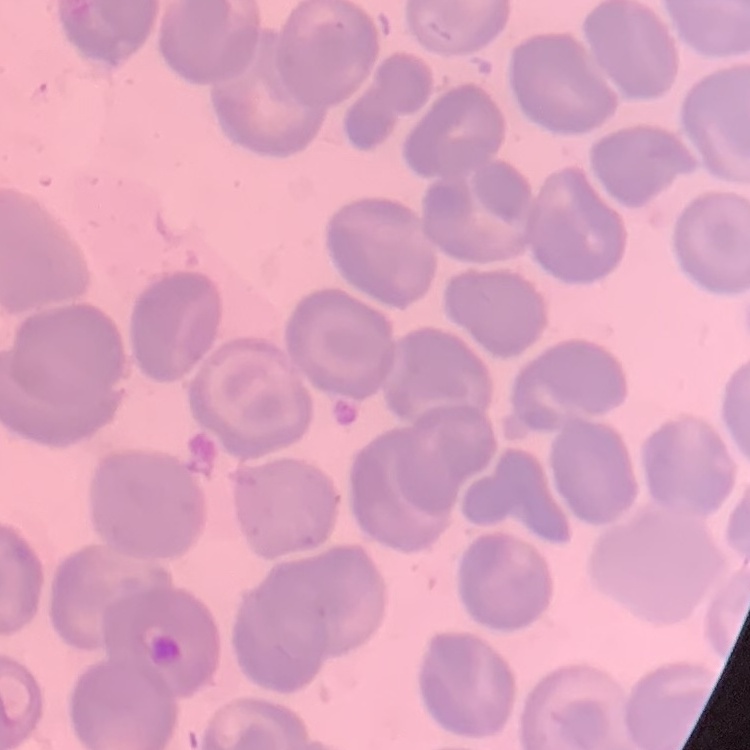

The red blood cells show no rouleaux formation. Thin blood film. Square crop of a larger photomicrograph. Stained with either Field's or Giemsa.